State the preparation type.
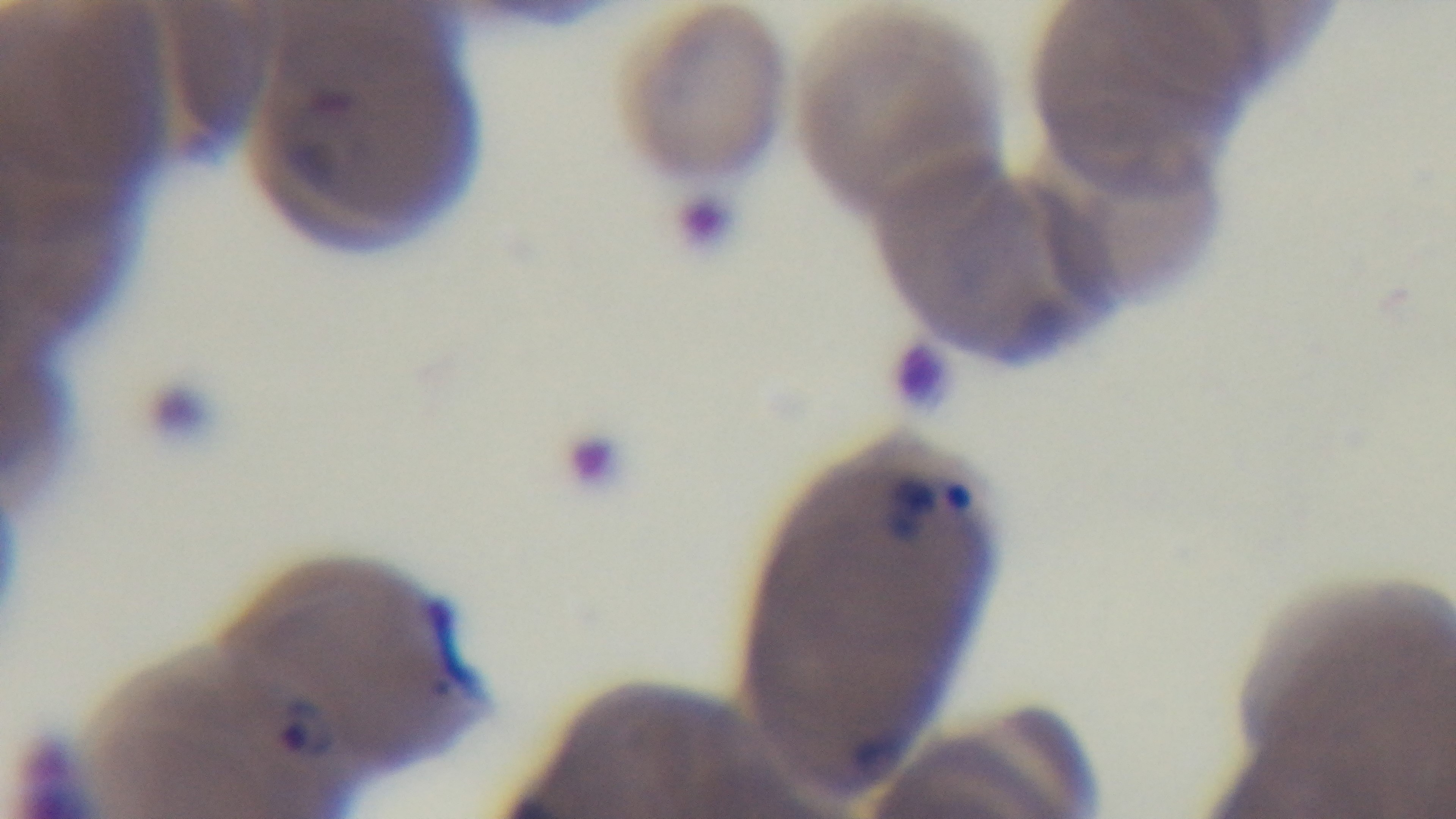
It is a thin blood film.

Summary:
  - Objective: 100x oil immersion
  - Malaria status: positive
  - Modality: light microscopy
  - Capture: mounted 4K digital camera
  - Stain: Giemsa
  - Field of view: one from the slide